Classify this cell by malaria status.
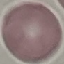
It is uninfected.

{
  "capture": "smartphone camera at the microscope eyepiece",
  "preparation": "thin smear",
  "stain": "Giemsa",
  "image_type": "automatically extracted cell patch, resized to 64 × 64 pixels"
}